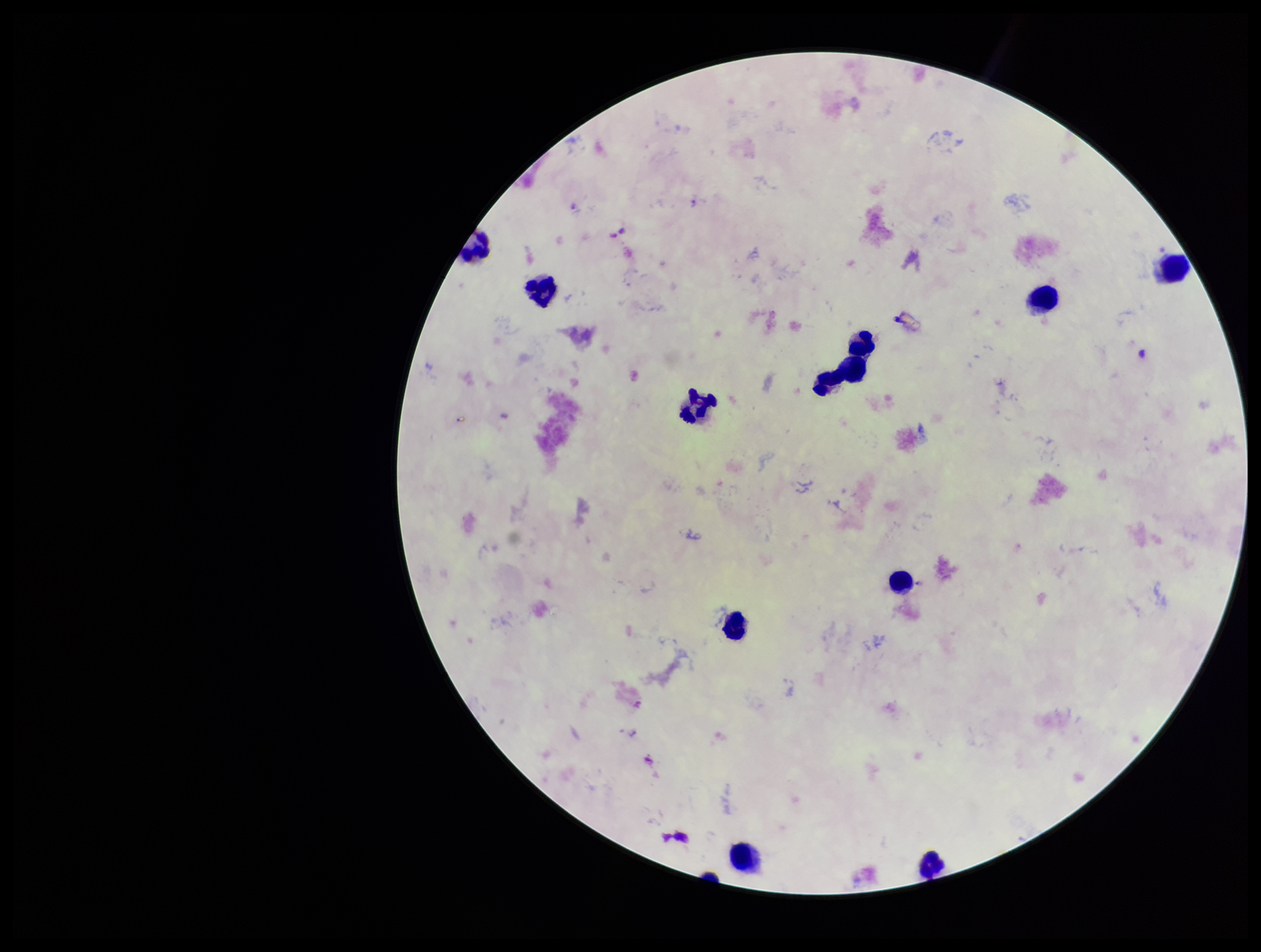

Summary:
  - Patient malaria status: positive
  - Plasmodium parasites: detected
  - Species reported for this patient: Plasmodium falciparum
  - Preparation: thick
  - Stain: Giemsa
  - Field of view: one from this slide
  - Capture: smartphone photograph through the microscope eyepiece
  - Image size: 1261×952 pixels
  - Parasite count: 3
  - Leukocyte count: 11